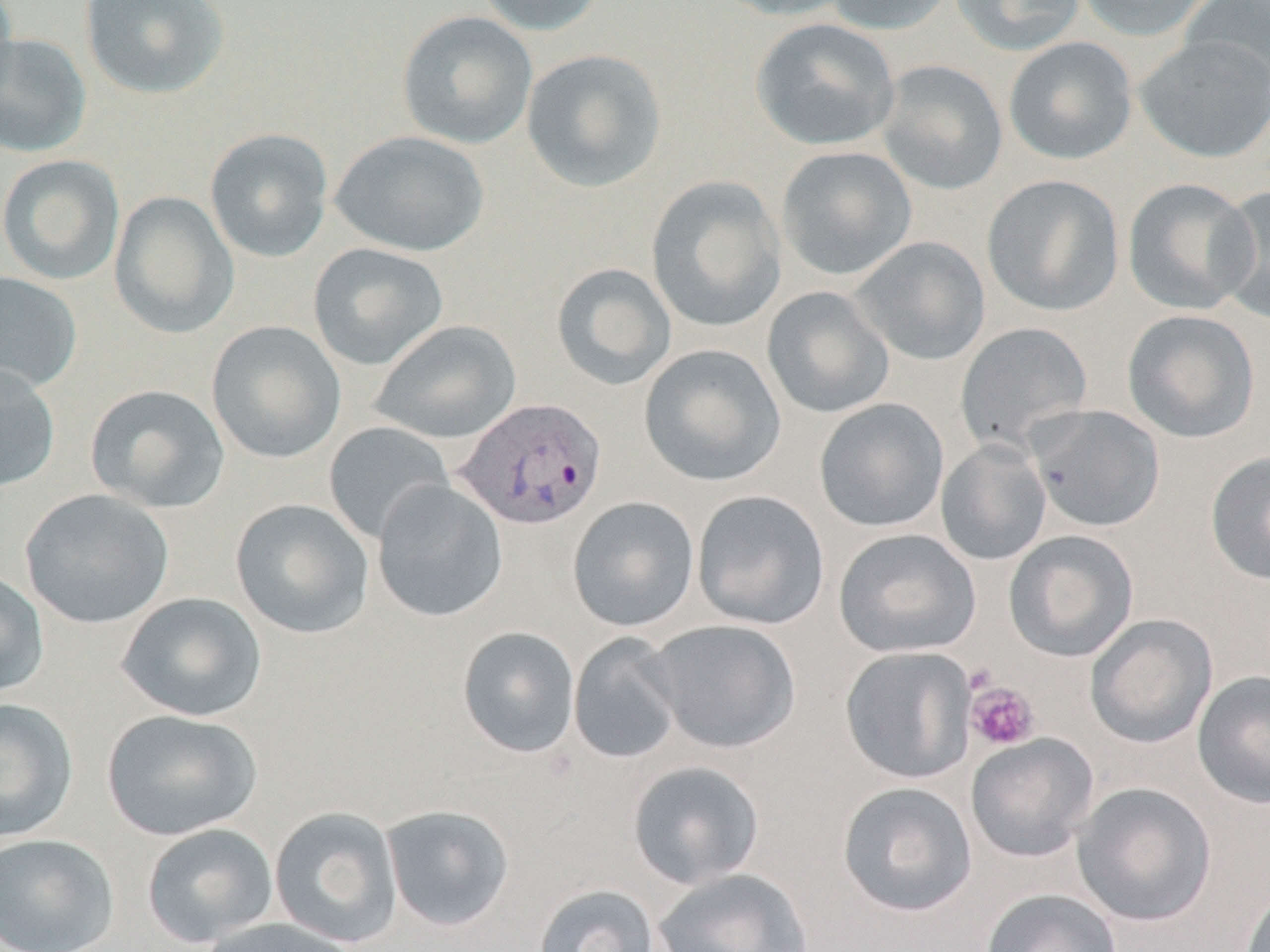
Summary:
  - Coordinate format: approximate bounding boxes as (x1,y1)-(x2,y2) corner pairs in pixels
  - Platelet locations: (965,680)-(1040,750)
  - Plasmodium vivax-infected red blood cell locations: (452,397)-(607,530)
  - Uninfected red blood cell locations: (0,0)-(19,103), (79,0)-(230,100), (474,0)-(608,37), (712,0)-(858,21), (822,0)-(958,35), (951,0)-(1088,56), (1075,0)-(1216,41), (1179,1)-(1269,94), (396,10)-(538,150), (750,17)-(900,152), (0,32)-(92,158), (1134,34)-(1270,163), (1003,36)-(1138,165), (521,49)-(668,193), (875,60)-(1008,196), (204,128)-(333,263), (329,130)-(490,257), (776,146)-(917,281), (0,154)-(125,285), (981,173)-(1124,317), (645,175)-(787,333), (1123,177)-(1260,315), (1213,184)-(1269,325), (109,191)-(239,339), (850,235)-(990,366), (308,242)-(448,371), (551,262)-(677,391), (0,271)-(82,394), (762,286)-(895,419), (1122,309)-(1261,443), (370,320)-(522,444), (205,321)-(346,464), (955,322)-(1093,457), (638,343)-(786,487), (0,364)-(61,492), (85,384)-(230,513), (814,398)-(949,533), (1026,404)-(1165,532), (323,421)-(454,544), (936,439)-(1052,566), (1205,450)-(1270,586), (372,480)-(508,623), (19,488)-(175,629), (691,490)-(829,630), (567,496)-(700,632), (230,498)-(374,639), (834,527)-(982,658), (1003,530)-(1139,662), (0,569)-(49,698), (116,592)-(268,722), (1085,614)-(1218,749), (647,619)-(801,753), (457,626)-(580,758), (567,632)-(684,765), (840,645)-(976,784), (1192,670)-(1270,809), (0,698)-(79,843), (101,709)-(262,841), (965,733)-(1099,863), (627,760)-(765,889), (836,781)-(978,918), (1072,782)-(1217,926), (380,804)-(515,932), (269,806)-(404,948), (141,822)-(279,948), (0,833)-(120,952), (651,867)-(814,952), (531,884)-(662,952), (1239,885)-(1270,952), (980,888)-(1122,952), (193,916)-(362,952)
  - Slide-level diagnosis: Plasmodium vivax
  - Image size: 1270×952 pixels
  - Field of view: single
  - Modality: light microscopy
  - Magnification: 1000x
  - Preparation: thin blood film
  - Stain: May-Grünwald-Giemsa